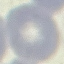

Summary:
  - Result: no malaria parasites seen
  - Capture: smartphone through the microscope eyepiece
  - Image type: automatically extracted cell patch, resized to 64 × 64 pixels
  - Stain: Giemsa
  - Preparation: thin smear